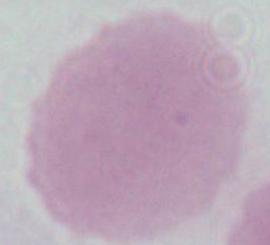
{
  "modality": "micrograph",
  "magnification": "1000x",
  "identification": "red blood cell"
}